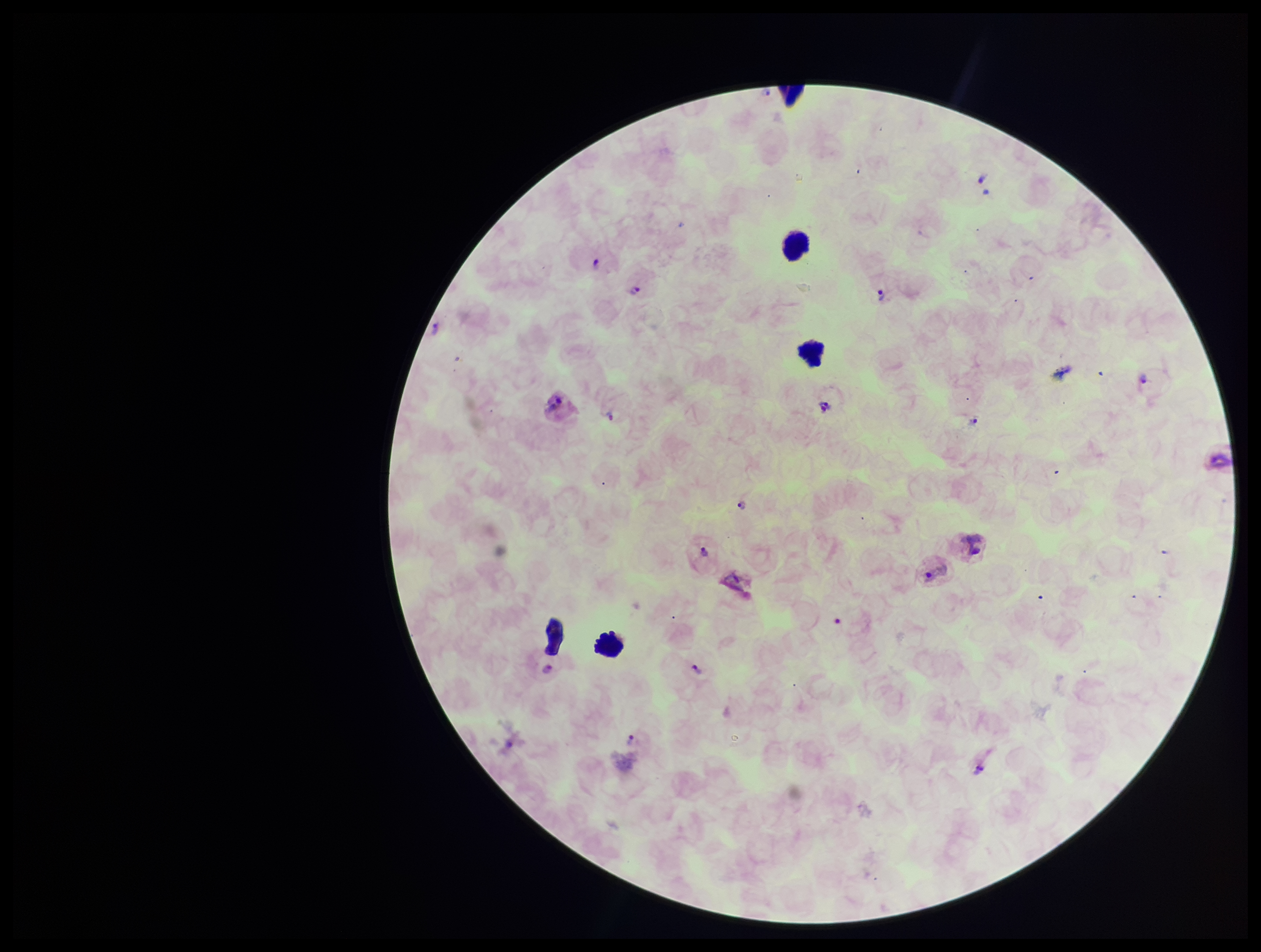

Summary:
  - Stain: Giemsa
  - Leukocyte count: 4
  - Capture: smartphone photograph through the microscope eyepiece
  - Image size: 1261×952 pixels
  - Preparation: thick blood smear
  - Patient malaria status: infected
  - Field of view: single
  - Species reported for this patient: Plasmodium vivax
  - Plasmodium parasites: detected
  - Parasite count: 13